State which cell type is depicted.
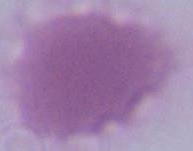

This is an erythrocyte.

Summary:
  - Modality: photomicrograph
  - Magnification: 1000x